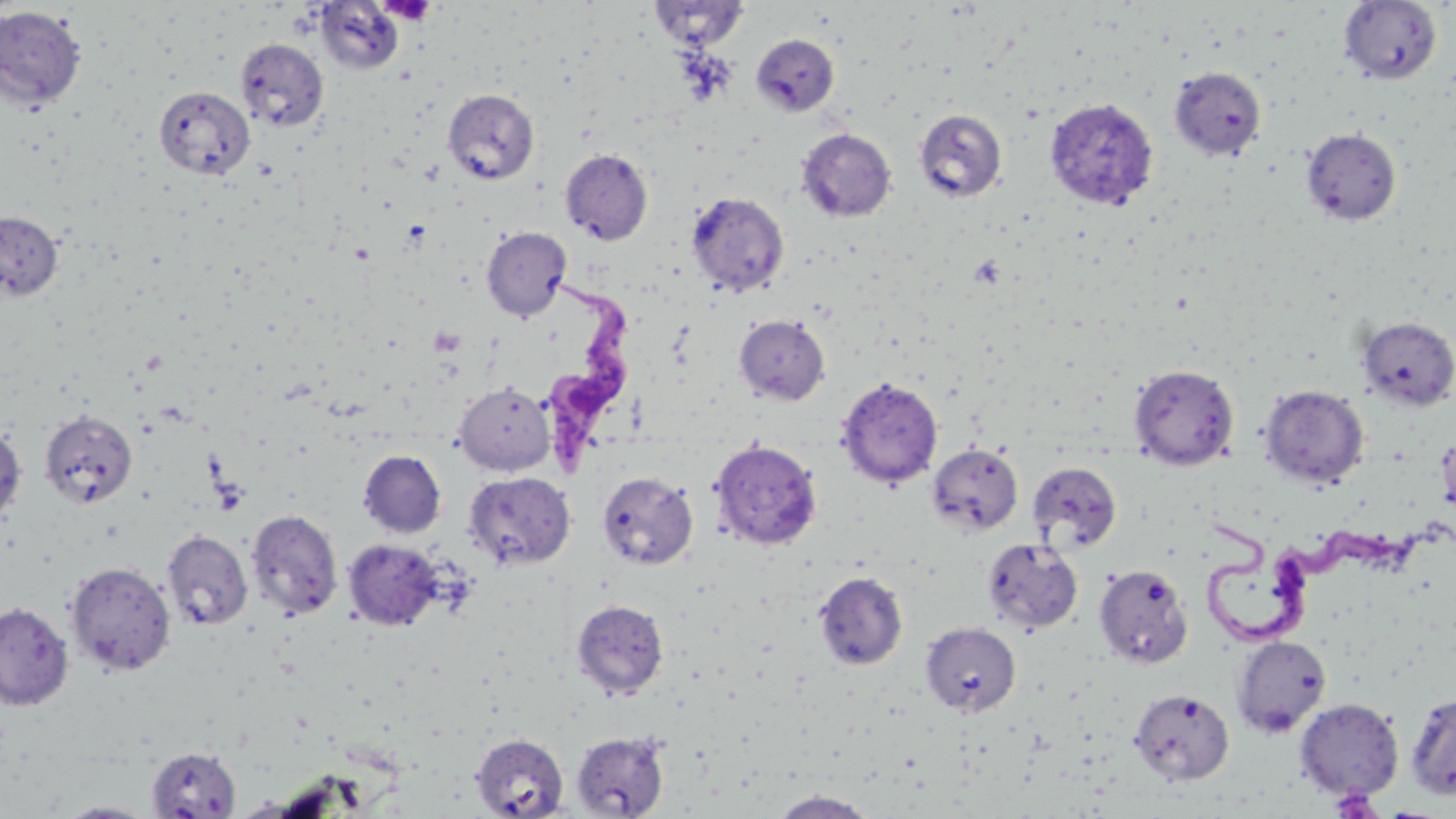
slide-level diagnosis = Trypanosoma brucei
magnification = 1000x
field of view = single
uninfected red blood cell locations = approximate bounding boxes as [x1, y1, x2, y2] in pixels: [315, 1, 404, 74], [648, 1, 751, 49], [1339, 1, 1443, 85], [0, 6, 86, 110], [750, 33, 841, 117], [235, 38, 329, 132], [1169, 66, 1267, 161], [154, 85, 255, 182], [443, 89, 539, 184], [1044, 97, 1158, 211], [914, 109, 1008, 202], [796, 128, 897, 222], [1301, 128, 1402, 225], [560, 148, 653, 245], [686, 192, 790, 297], [0, 211, 63, 301], [481, 226, 571, 321], [734, 314, 830, 405], [1357, 316, 1456, 411], [1129, 364, 1240, 471], [837, 377, 943, 488], [454, 381, 555, 475], [1259, 384, 1370, 489], [39, 409, 137, 509], [0, 422, 27, 526], [1437, 428, 1456, 520], [710, 439, 823, 550], [927, 444, 1023, 536], [358, 450, 447, 538], [1028, 461, 1122, 555], [464, 471, 576, 570], [597, 471, 698, 569], [246, 509, 343, 620], [162, 530, 253, 630], [982, 537, 1083, 633], [343, 538, 444, 631], [66, 562, 176, 676], [1094, 564, 1193, 669], [814, 571, 908, 670], [571, 599, 669, 699], [0, 602, 74, 710], [920, 621, 1021, 716], [1231, 635, 1331, 737], [1129, 688, 1235, 785], [1404, 690, 1456, 801], [1294, 698, 1404, 801], [570, 731, 669, 817], [470, 732, 569, 818], [147, 745, 242, 818], [768, 789, 881, 818], [53, 801, 161, 817]
platelet locations = approximate bounding boxes as [x1, y1, x2, y2] in pixels: [378, 0, 436, 25], [970, 254, 1005, 288]
stain = May-Grünwald-Giemsa
Trypanosoma brucei locations = approximate bounding boxes as [x1, y1, x2, y2] in pixels: [544, 278, 637, 471], [1192, 514, 1409, 643]
preparation = thin blood film
modality = light microscopy
image size = 1456×819 pixels